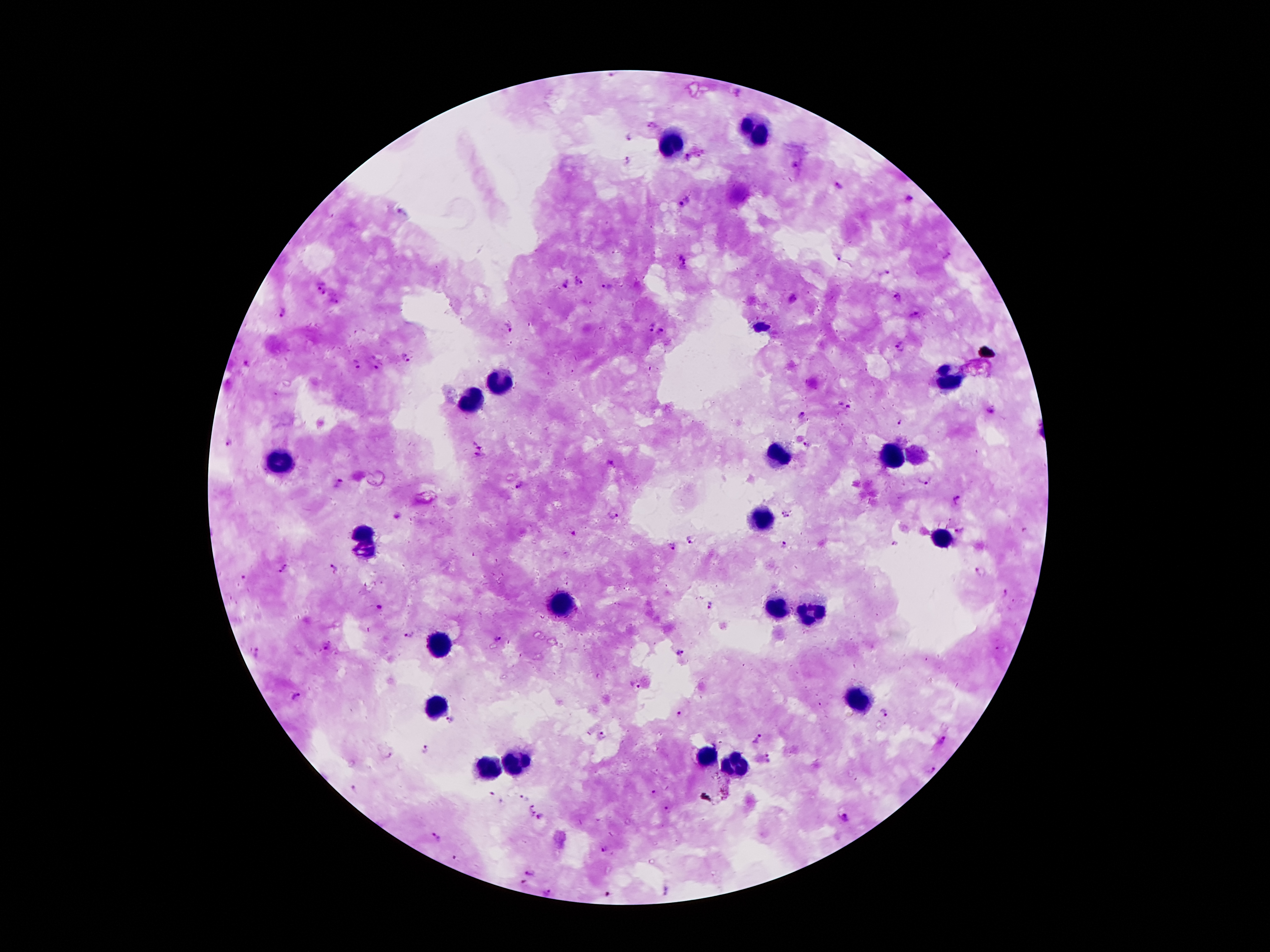
One field from this slide. Thick peripheral-blood smear. Giemsa stain. 100x magnification. Image is 1270×952 pixels. Smartphone photograph taken through the microscope eyepiece. Patient malaria status: positive for Plasmodium falciparum.